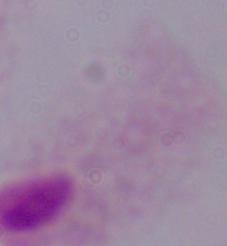
magnification = 1000x
modality = photomicrograph
identification = trichomonad